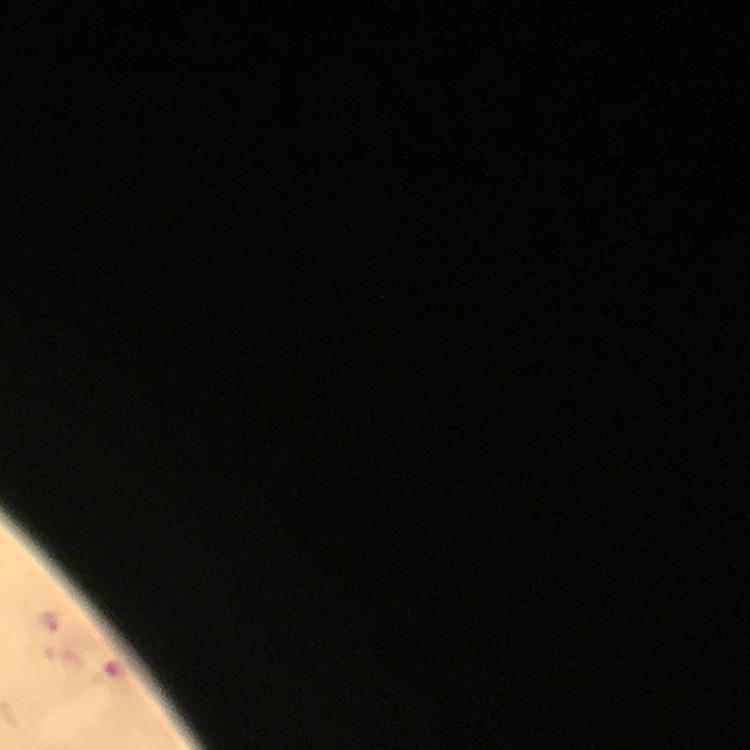

Approximate centers as [x, y] in pixels. Malaria parasite locations: [47, 621]. Giemsa stain. Cropped region of a single field of view. At 100x magnification. Immersion oil applied. Thick smear. Photographed with a smartphone mounted on the microscope. From a malaria diagnostic workup. Image is 750×750 pixels.